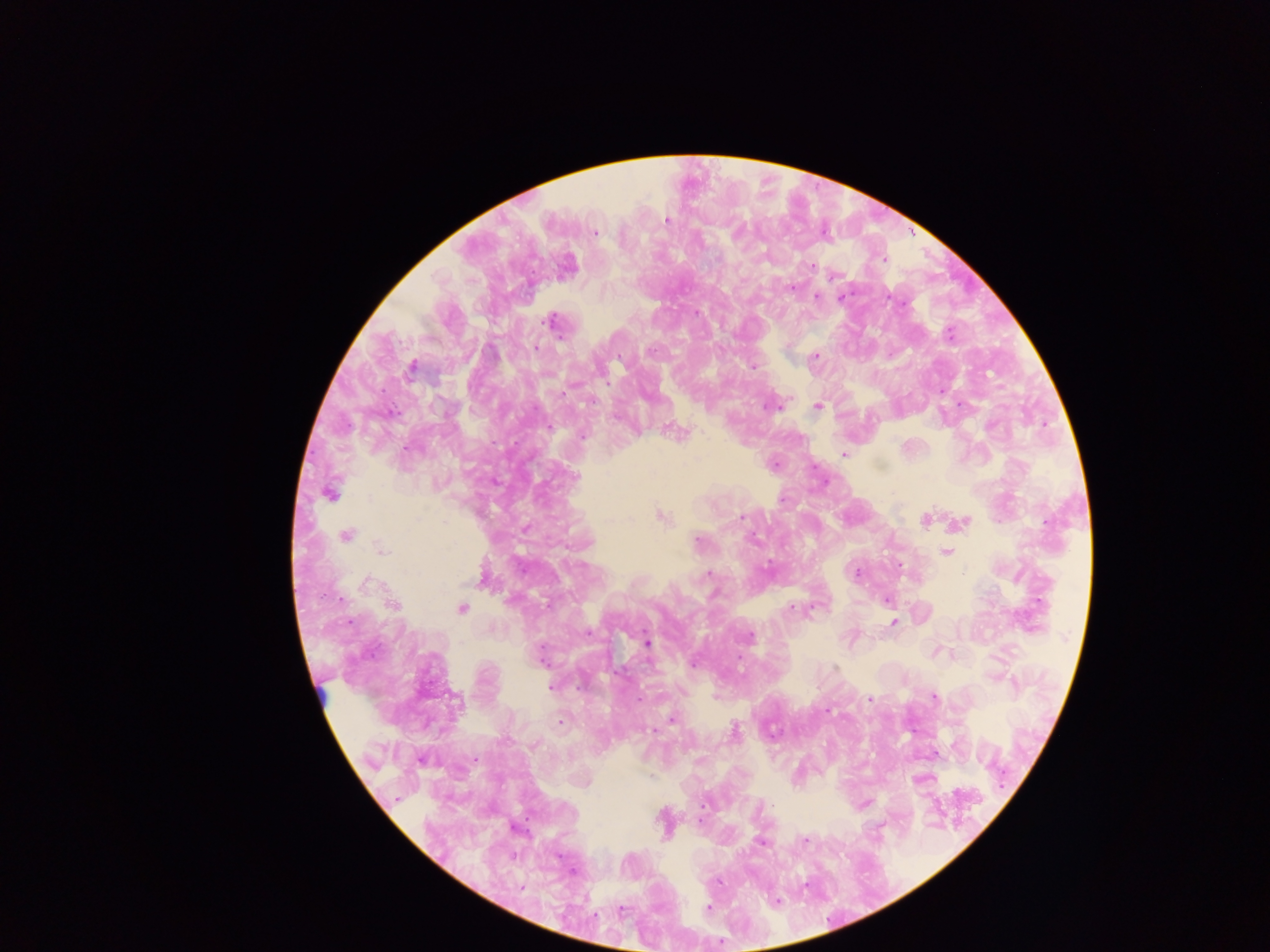
preparation = thick blood film
malaria parasite locations = approximate centers as (x, y) in pixels: (665, 220), (595, 232), (738, 232), (884, 259), (810, 266), (831, 277), (792, 287), (816, 297), (841, 297), (697, 313), (549, 321), (949, 334), (536, 348), (650, 351), (814, 357), (752, 366), (412, 368), (769, 407), (817, 407), (550, 427), (582, 436), (844, 454), (774, 464), (576, 476), (329, 494), (660, 516), (740, 517), (924, 520), (962, 522), (346, 535), (752, 539), (697, 540), (381, 550), (946, 553), (899, 565), (768, 567), (856, 573), (963, 573), (709, 574), (483, 579), (366, 582), (886, 601), (393, 605), (461, 608), (792, 609), (893, 622), (750, 636), (647, 643), (694, 664), (551, 687), (580, 687), (934, 698), (639, 699), (869, 699), (828, 711), (671, 720), (561, 722), (653, 730), (734, 730), (475, 759), (805, 840), (761, 843), (718, 882), (521, 888), (709, 908), (621, 910)
leukocyte locations = approximate centers as (x, y) in pixels (subset; some below the resolvable size): (321, 692)
country = Ghana
image size = 1270×952 pixels
field of view = single
capture = mobile-phone photograph through a microscope